Report the malaria status of this cell.
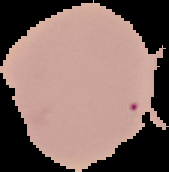

Uninfected.

{
  "image_size": "169×172 pixels",
  "image_type": "segmented cell region on a black background",
  "preparation": "thin blood film"
}